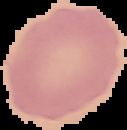

Summary:
  - Image type: segmented cell region with the area outside set to black
  - Preparation: thin blood film
  - Image size: 127×130 pixels
  - Result: no malaria parasites detected